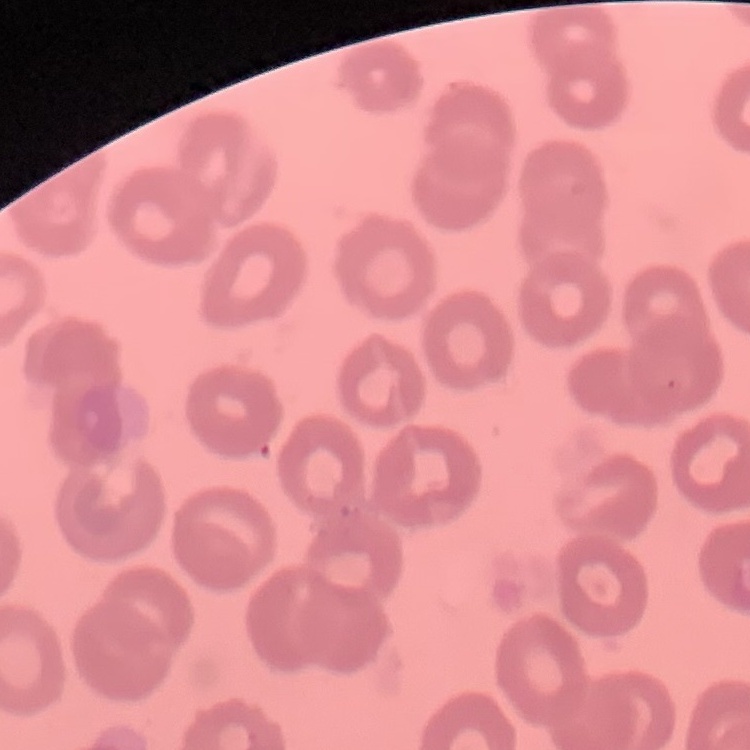

Summary:
  - Red blood cell morphology: no rouleaux formation
  - Preparation: thin peripheral smear
  - Image type: one tile cut from a larger photomicrograph
  - Stain: Field's or Giemsa